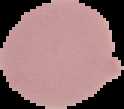

The area outside the segmented cell region is set to black. Image is 124×109 pixels. Malaria status: uninfected. From a thin blood film.